Classify this cell by malaria status.
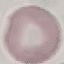

Uninfected.

Summary:
  - Stain: Giemsa
  - Image type: cell patch, automatically extracted from a larger field of view and resized to 64 × 64 pixels
  - Preparation: thin blood film
  - Capture: smartphone through the microscope eyepiece